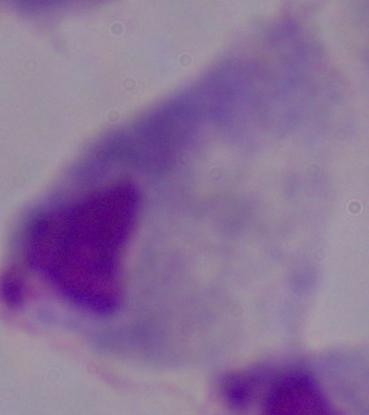
Summary:
  - Magnification: 1000x
  - Modality: photomicrograph
  - Identification: trichomonad